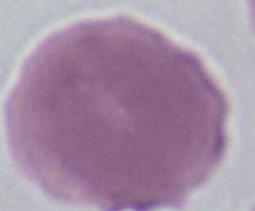

Captured at 1000x magnification. An erythrocyte is seen. Photomicrograph.